Classify this cell by malaria status.
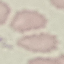

Uninfected.

Summary:
  - Image type: cell patch, automatically extracted from a larger field of view and resized to 64 × 64 pixels
  - Capture: smartphone camera at the microscope eyepiece
  - Stain: Giemsa
  - Preparation: thin blood smear